Report the malaria status of this cell.
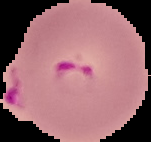
Parasitized.

Summary:
  - Image type: segmented cell region with the area outside set to black
  - Image size: 151×142 pixels
  - Preparation: thin blood smear